Name the parasite shown.
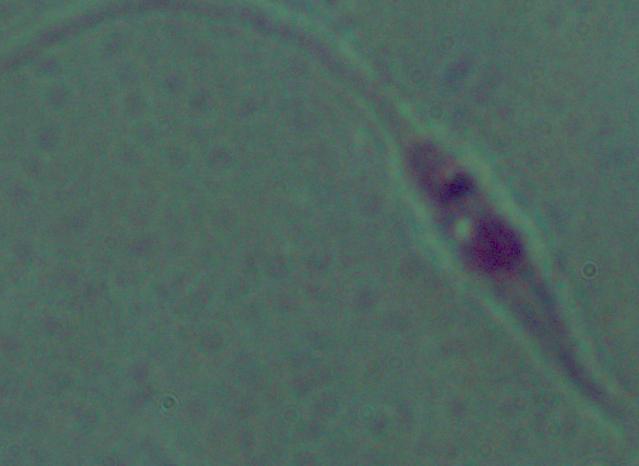
Leishmania.

Captured at 1000x magnification. Photomicrograph.